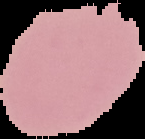
image_type: segmented cell region with the area outside set to black
malaria_status: uninfected
image_size: 145×139 pixels
preparation: thin blood film